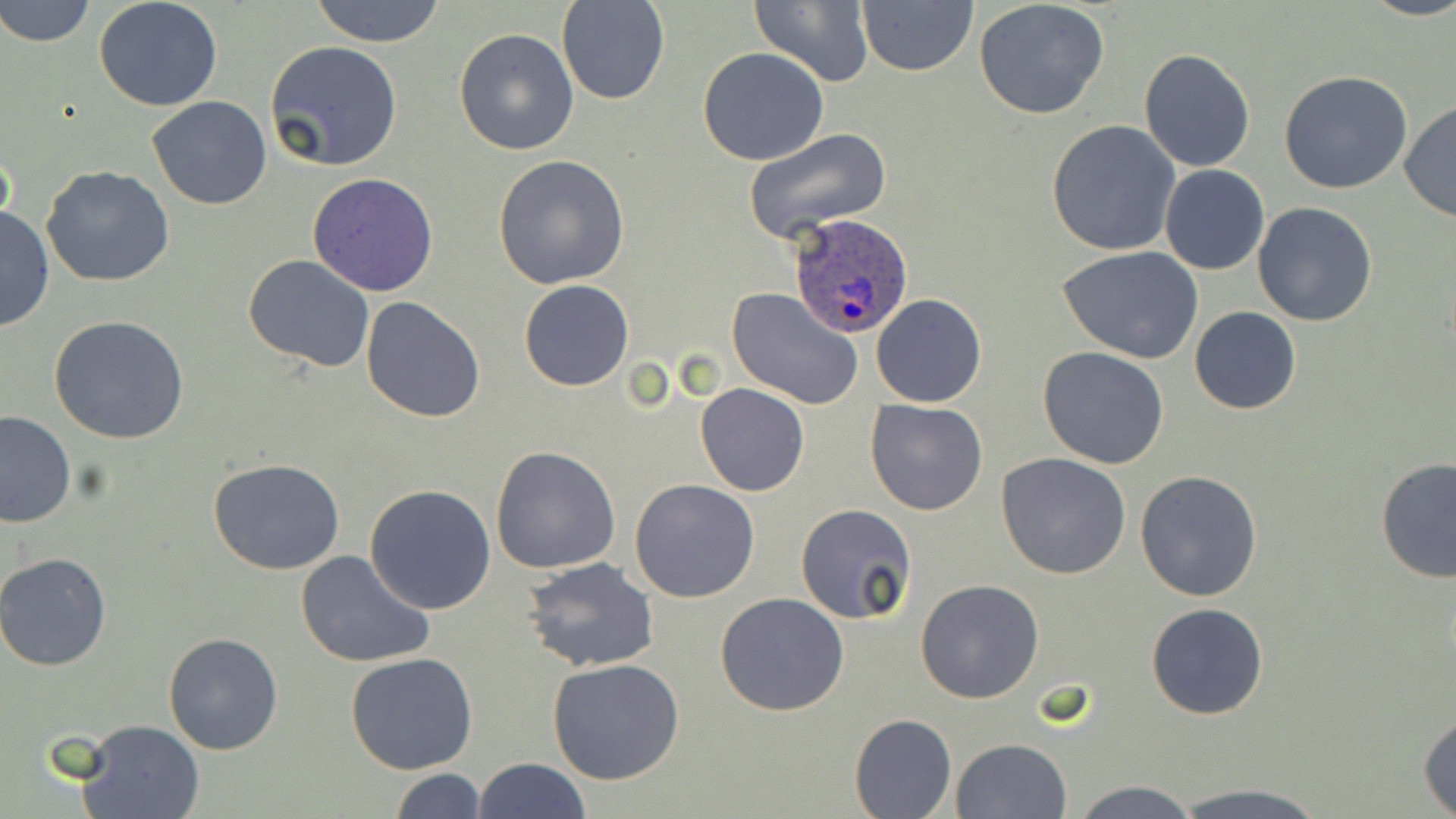
slide-level diagnosis = Plasmodium ovale
stain = May-Grünwald-Giemsa
modality = optical microscopy
Plasmodium ovale-infected red blood cell locations = approximate bounding boxes as (x1, y1, x2, y2) in pixels: (789, 211, 916, 338)
field of view = single
image size = 1456×819 pixels
uninfected red blood cell locations = approximate bounding boxes as (x1, y1, x2, y2) in pixels: (1, 0, 95, 47), (94, 0, 222, 111), (310, 0, 447, 47), (557, 0, 670, 105), (856, 0, 978, 77), (974, 0, 1109, 120), (1359, 0, 1456, 22), (751, 1, 873, 85), (454, 27, 580, 156), (265, 39, 404, 172), (697, 46, 830, 166), (1138, 47, 1255, 173), (1278, 71, 1412, 194), (148, 95, 272, 209), (1400, 101, 1456, 223), (1045, 119, 1181, 256), (742, 128, 891, 244), (493, 154, 630, 289), (41, 164, 175, 288), (1160, 165, 1269, 275), (307, 173, 439, 296), (1253, 202, 1378, 326), (0, 207, 53, 333), (1058, 245, 1205, 365), (244, 254, 375, 370), (519, 279, 634, 391), (726, 288, 864, 410), (872, 294, 987, 408), (361, 296, 487, 422), (1190, 307, 1300, 414), (49, 315, 189, 445), (1038, 345, 1169, 468), (695, 382, 809, 497), (865, 399, 990, 516), (0, 410, 75, 526), (490, 446, 620, 573), (997, 452, 1132, 578), (1376, 458, 1456, 585), (208, 459, 345, 574), (1134, 470, 1262, 602), (630, 479, 761, 604), (364, 484, 497, 615), (795, 503, 919, 625), (295, 549, 434, 669), (0, 552, 112, 671), (523, 557, 660, 673), (914, 579, 1043, 704), (716, 592, 849, 716), (1146, 602, 1270, 719), (163, 632, 284, 755), (346, 653, 478, 774), (546, 659, 686, 786), (1418, 710, 1456, 814), (849, 713, 956, 818), (75, 718, 204, 819), (951, 738, 1071, 819), (473, 758, 590, 818), (391, 768, 485, 819), (1069, 780, 1204, 819), (1171, 784, 1332, 819)
magnification = 1000x
preparation = thin blood film